Classify this cell by malaria status.
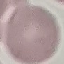

It is uninfected.

Automatically extracted cell patch, resized to 64 × 64 pixels. Photographed with a smartphone camera at the microscope eyepiece. Thin blood film. Giemsa stain.